Name the blood parasite species.
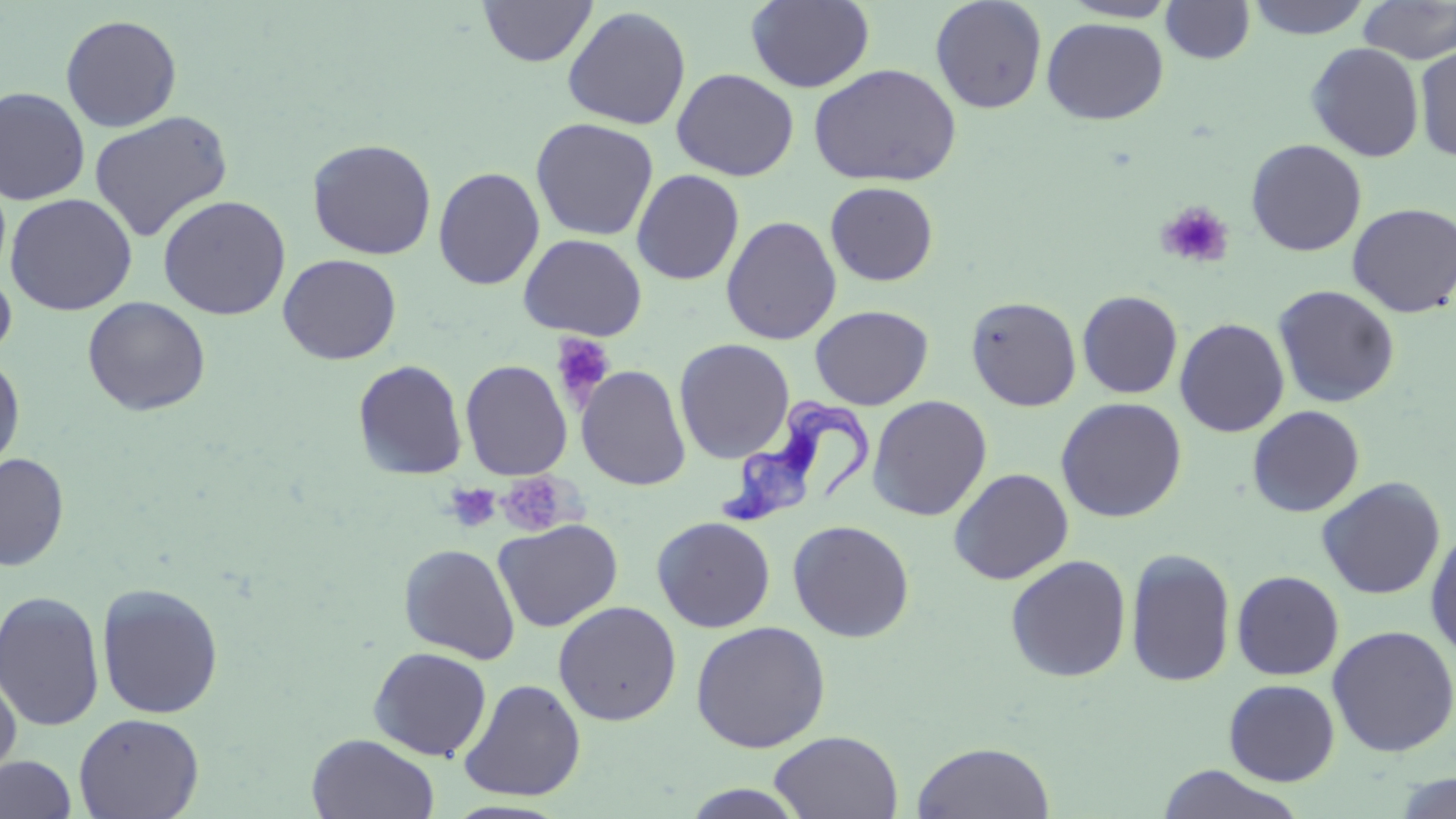

Trypanosoma brucei.

field of view = single
uninfected red blood cell locations = approximate bounding boxes as [x1, y1, x2, y2] in pixels: [746, 0, 875, 92], [930, 0, 1047, 113], [1060, 0, 1180, 22], [1245, 0, 1373, 39], [478, 1, 598, 67], [1160, 1, 1256, 64], [1357, 1, 1456, 64], [562, 6, 692, 130], [60, 13, 182, 132], [1041, 17, 1169, 125], [1306, 42, 1424, 162], [1414, 45, 1456, 162], [808, 63, 962, 187], [671, 68, 799, 181], [0, 86, 91, 205], [88, 110, 234, 242], [530, 117, 659, 241], [307, 138, 437, 260], [1246, 139, 1367, 256], [433, 166, 545, 290], [631, 169, 745, 285], [825, 181, 939, 286], [4, 193, 138, 316], [157, 194, 291, 320], [1347, 202, 1456, 318], [720, 215, 842, 345], [518, 233, 647, 340], [278, 253, 402, 364], [0, 264, 17, 363], [1272, 284, 1401, 408], [1077, 290, 1183, 399], [966, 296, 1082, 411], [83, 297, 211, 416], [810, 304, 933, 410], [1174, 317, 1290, 437], [674, 338, 795, 464], [0, 353, 25, 475], [352, 360, 468, 481], [460, 360, 572, 480], [576, 365, 691, 491], [867, 395, 992, 521], [1055, 397, 1187, 522], [1247, 405, 1365, 517], [0, 453, 70, 571], [949, 467, 1074, 584], [1316, 477, 1445, 599], [652, 516, 775, 632], [493, 518, 623, 632], [787, 519, 915, 642], [1425, 528, 1456, 660], [398, 542, 521, 664], [1125, 547, 1236, 688], [1004, 554, 1132, 683], [1231, 570, 1344, 680], [96, 582, 225, 719], [0, 589, 106, 732], [553, 601, 681, 726], [690, 621, 831, 753], [1326, 624, 1456, 758], [367, 647, 492, 760], [0, 666, 22, 787], [458, 678, 586, 802], [1223, 679, 1340, 786], [73, 712, 204, 819], [770, 730, 903, 817], [306, 733, 440, 818], [911, 741, 1056, 819], [0, 755, 77, 819], [1155, 765, 1305, 819], [1390, 773, 1456, 818], [679, 784, 810, 818]
stain = May-Grünwald-Giemsa
image size = 1456×819 pixels
magnification = 1000x
preparation = thin blood film
Trypanosoma brucei locations = approximate bounding boxes as [x1, y1, x2, y2] in pixels: [719, 398, 875, 531]
platelet locations = approximate bounding boxes as [x1, y1, x2, y2] in pixels: [1157, 201, 1235, 269], [551, 333, 615, 407], [495, 473, 574, 535], [445, 483, 502, 533]
modality = optical microscopy